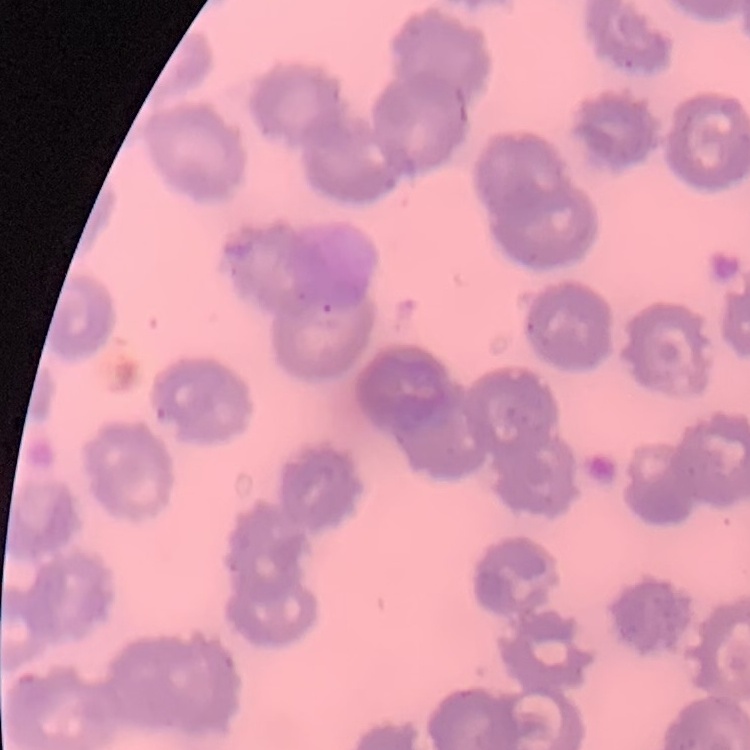
red blood cell morphology = no rouleaux formation
image type = square crop of a larger photomicrograph
preparation = thin blood film
stain = Field's or Giemsa